Comment on the morphology of the red blood cells.
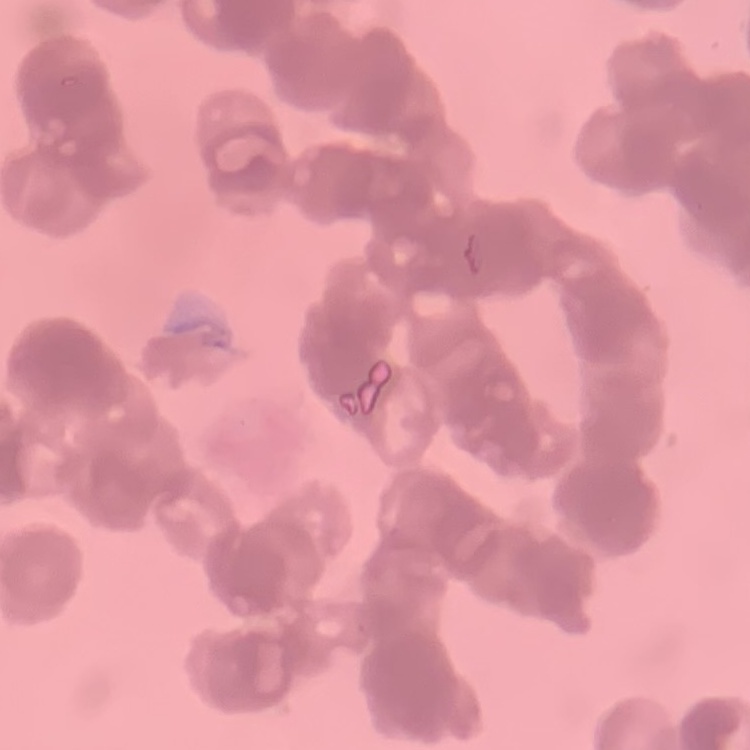

Rouleaux formation.

Field's or Giemsa stain. Thin peripheral smear. Square crop of a larger photomicrograph.